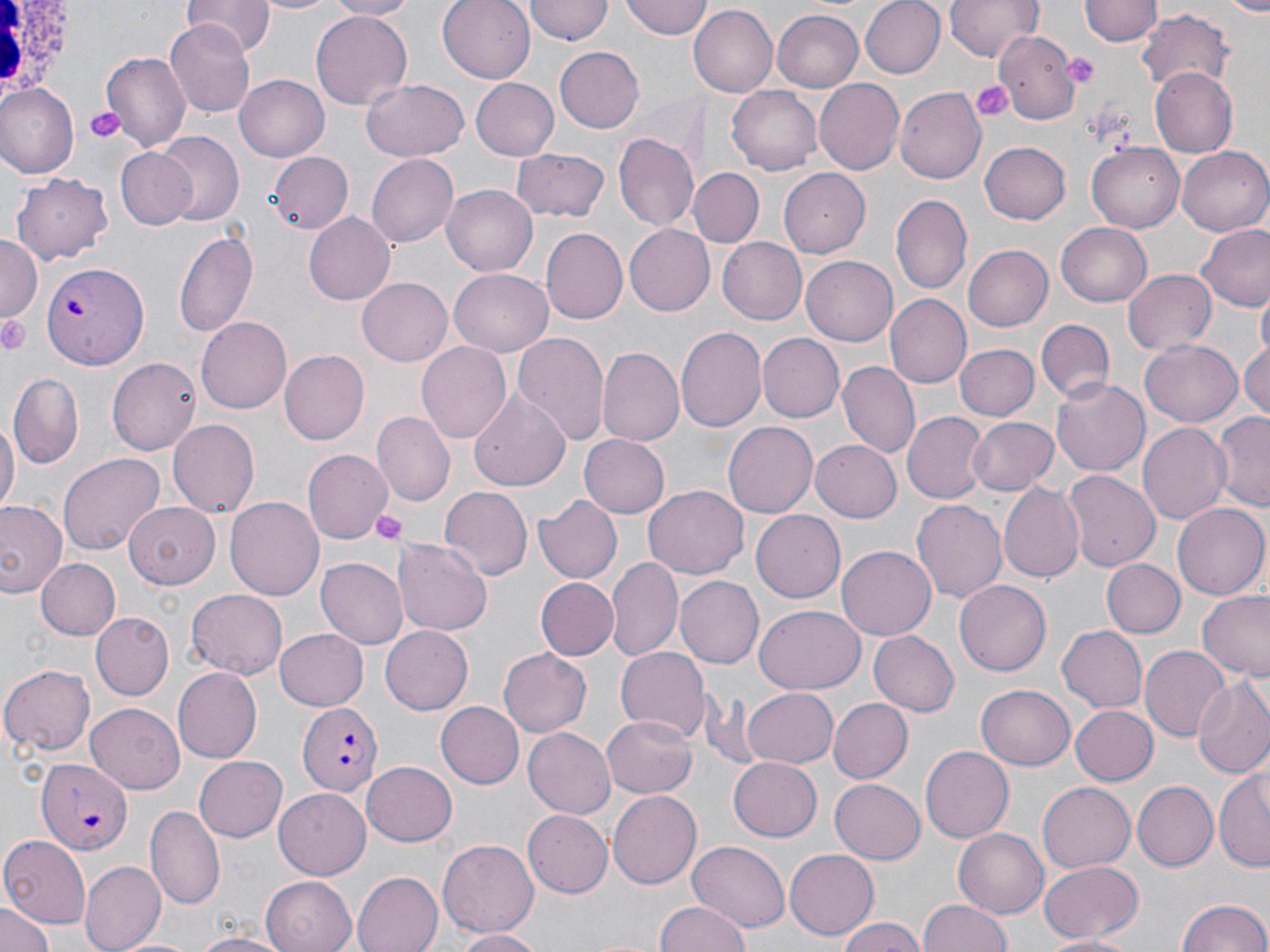

{
  "slide_level_diagnosis": "Plasmodium falciparum",
  "uninfected_red_blood_cell_locations": "approximate bounding boxes as (x1,y1)-(x2,y2) corner pairs in pixels: (182,0)-(273,53), (251,0)-(344,16), (324,0)-(421,20), (438,0)-(534,83), (619,0)-(712,38), (858,0)-(945,79), (945,0)-(1042,63), (1080,0)-(1159,48), (1226,0)-(1270,13), (524,1)-(612,45), (692,6)-(777,98), (772,9)-(865,91), (1136,9)-(1234,91), (311,11)-(413,110), (165,20)-(257,116), (993,32)-(1082,118), (115,36)-(245,132), (555,47)-(644,134), (102,54)-(190,151), (1150,69)-(1236,155), (234,75)-(327,161), (469,76)-(559,159), (361,79)-(469,163), (815,79)-(905,174), (3,85)-(78,178), (727,85)-(824,174), (897,88)-(986,183), (614,133)-(699,234), (152,135)-(243,227), (978,141)-(1070,224), (1086,143)-(1185,232), (512,146)-(609,221), (115,148)-(198,231), (1177,148)-(1270,235), (267,151)-(353,236), (367,153)-(458,248), (779,167)-(874,257), (689,168)-(763,248), (12,173)-(115,265), (442,184)-(539,276), (890,195)-(971,296), (304,212)-(399,305), (1055,222)-(1152,307), (1197,223)-(1270,312), (626,225)-(714,315), (173,228)-(258,341), (540,229)-(627,325), (0,235)-(39,323), (715,236)-(807,325), (809,245)-(903,432), (963,245)-(1053,331), (801,253)-(897,343), (1123,268)-(1216,357), (448,269)-(553,354), (358,279)-(452,365), (1256,288)-(1269,359), (884,296)-(970,390), (197,315)-(292,412), (1037,318)-(1114,403), (676,326)-(766,434), (513,333)-(609,449), (758,333)-(844,421), (1239,336)-(1270,422), (1141,340)-(1243,427), (418,342)-(512,445), (953,344)-(1037,422), (598,346)-(683,445), (278,349)-(368,444), (107,357)-(201,456), (838,362)-(920,459), (8,374)-(82,465), (1050,376)-(1150,477), (467,385)-(573,496), (901,410)-(989,505), (1211,411)-(1270,512), (375,412)-(454,504), (966,417)-(1060,496), (0,419)-(17,515), (169,419)-(259,521), (1137,419)-(1231,528), (723,421)-(817,520), (581,433)-(670,519), (811,437)-(904,521), (302,449)-(391,544), (58,452)-(165,555), (1063,470)-(1160,572), (997,483)-(1085,585), (643,486)-(748,579), (438,487)-(530,581), (534,493)-(622,584), (227,496)-(323,601), (912,497)-(1008,605), (0,499)-(67,600), (125,502)-(220,587), (1173,503)-(1269,600), (751,508)-(846,600), (394,538)-(492,636), (837,545)-(937,640), (607,556)-(684,664), (35,558)-(122,640), (317,558)-(407,647), (1102,559)-(1186,638), (676,575)-(764,669), (536,577)-(617,660), (955,579)-(1051,676), (186,589)-(289,680), (1196,591)-(1270,678), (755,606)-(864,693), (90,612)-(173,700), (1057,625)-(1147,712), (381,627)-(473,715), (276,628)-(371,710), (869,630)-(959,716), (1139,644)-(1229,744), (612,645)-(708,743), (498,648)-(592,736), (0,664)-(96,755), (171,667)-(261,762), (1191,678)-(1270,779), (977,685)-(1076,770), (740,687)-(839,769), (826,698)-(912,783), (86,702)-(185,792), (436,702)-(523,789), (1070,705)-(1157,785), (601,712)-(696,798), (523,728)-(618,818), (922,746)-(1014,842), (194,754)-(287,842), (727,756)-(820,840), (361,761)-(456,846), (1216,761)-(1270,875), (829,778)-(926,864), (1133,780)-(1218,869), (1038,781)-(1136,872), (274,788)-(371,879), (608,791)-(701,888), (145,804)-(225,911), (522,810)-(611,897), (953,829)-(1048,918), (0,835)-(91,929), (686,839)-(791,930), (439,840)-(538,938), (785,850)-(879,939), (1038,860)-(1144,941), (80,861)-(165,951), (353,872)-(443,952), (261,875)-(358,952), (1177,897)-(1268,952), (0,898)-(53,952), (656,899)-(753,952), (916,900)-(1016,952), (835,916)-(929,952), (453,929)-(550,951), (189,931)-(292,952), (1041,935)-(1143,952)",
  "preparation": "thin blood film",
  "plasmodium_falciparum_infected_red_blood_cell_locations": "approximate bounding boxes as (x1,y1)-(x2,y2) corner pairs in pixels: (40,262)-(149,369), (296,700)-(382,793), (36,756)-(133,855)",
  "stain": "May-Grünwald-Giemsa",
  "image_size": "1270×952 pixels",
  "white_blood_cell_locations": "approximate bounding boxes as (x1,y1)-(x2,y2) corner pairs in pixels: (0,0)-(80,100)",
  "modality": "optical microscopy",
  "platelet_locations": "approximate bounding boxes as (x1,y1)-(x2,y2) corner pairs in pixels: (1066,52)-(1098,87), (970,79)-(1014,124), (83,105)-(124,145), (0,313)-(33,356), (369,508)-(409,545)",
  "magnification": "1000x",
  "field_of_view": "one of a larger specimen"
}